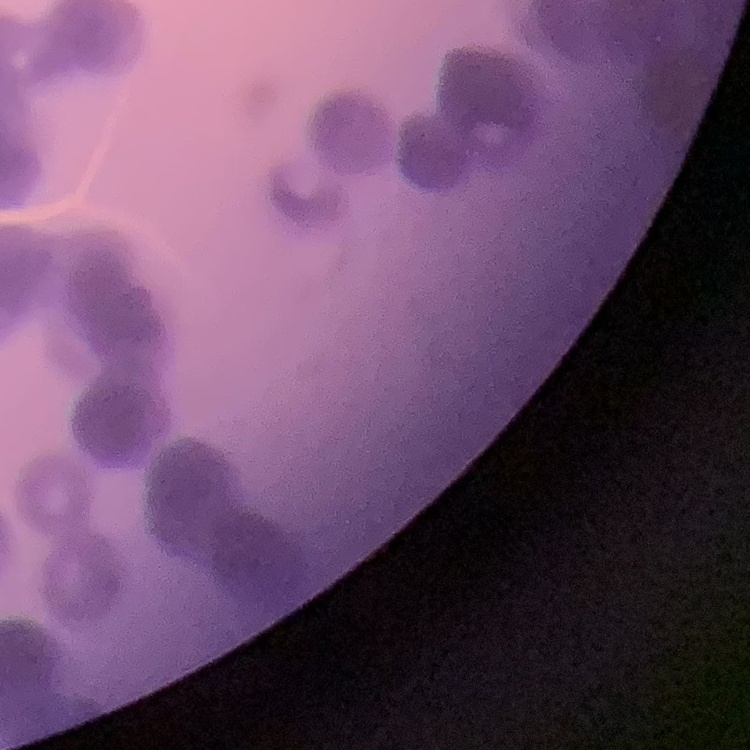

red blood cell morphology = rouleaux formation
preparation = thin peripheral smear
image type = square crop of a larger photomicrograph
stain = Field's or Giemsa